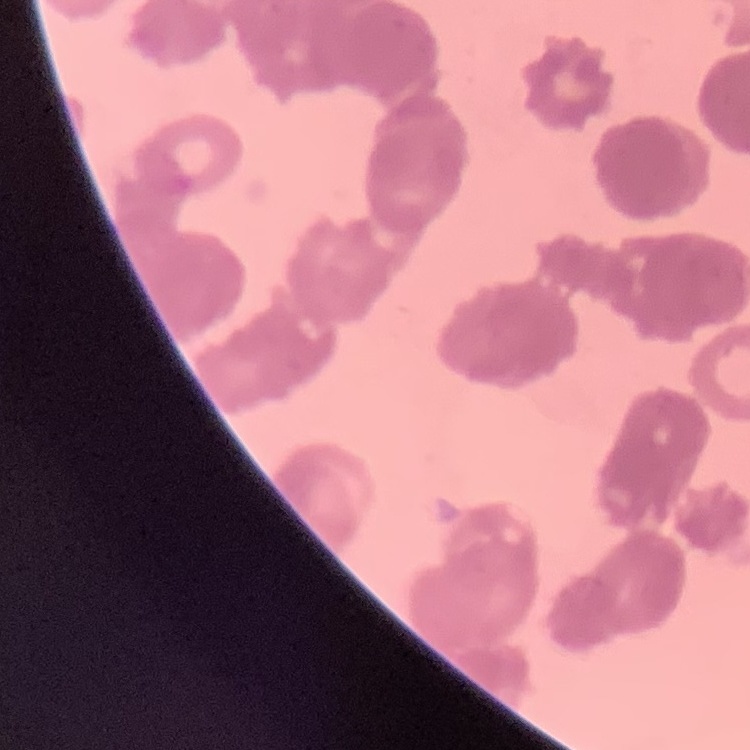
red blood cell morphology = rouleaux formation
image type = square crop of a larger photomicrograph
preparation = thin peripheral smear
stain = Field's or Giemsa